Give the position of each Plasmodium falciparum parasite with its life-cycle stage, each leukocyte, and any debris.
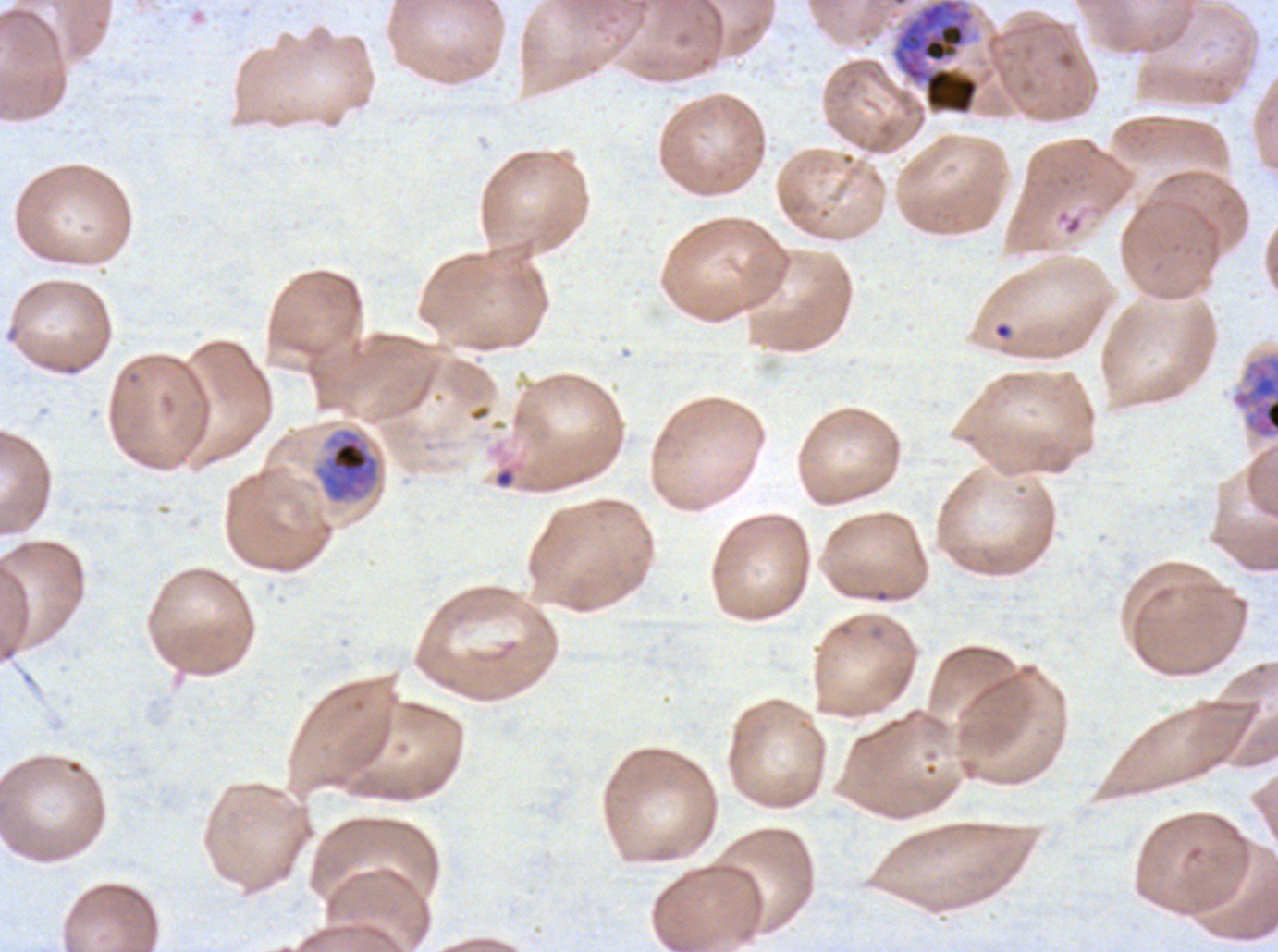
Approximate bounding boxes as [x1, y1, x2, y2] in pixels.
Rings: [993, 322, 1012, 339].
Early schizonts: [891, 0, 980, 116], [1230, 350, 1277, 441], [313, 428, 380, 504].
Debris: [891, 0, 980, 116] (two touching objects share this one region), [494, 467, 515, 489].
No late-ring/early-trophozoite forms, mid trophozoites, late trophozoites, late schizonts, segmenters, gametocytes, or leukocytes observed.

Thin blood smear. Giemsa-stained preparation. Ex-vivo Plasmodium falciparum culture from a patient in The Gambia, grown for 24 to 48 hours. Life-cycle stages observed: ring, early schizont. Image is 1278×952 pixels. One sub-image of a larger composite.